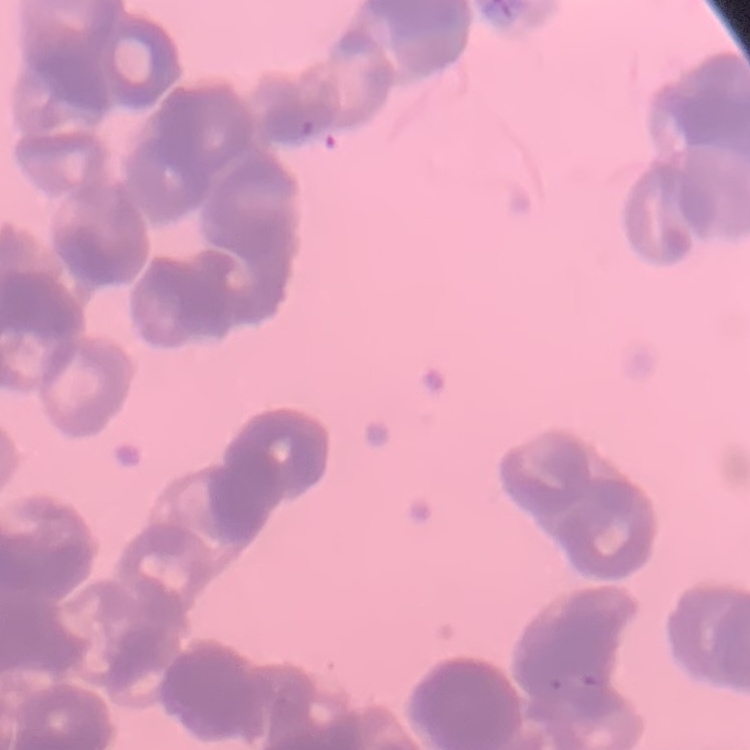
Summary:
  - Erythrocyte morphology: rouleaux formation
  - Image type: square crop of a larger photomicrograph
  - Stain: Field's or Giemsa
  - Preparation: thin peripheral smear